Describe the morphology of the erythrocytes.
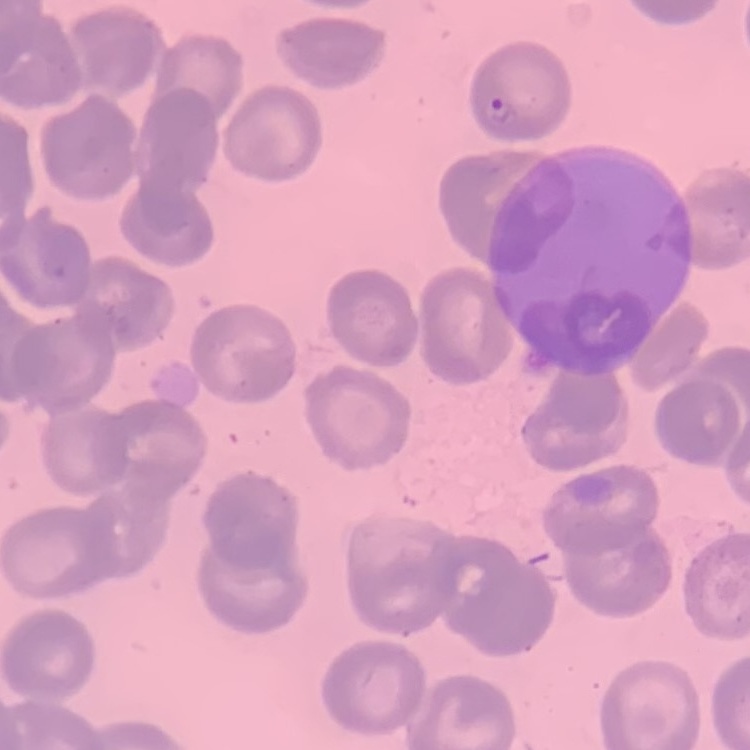

They show no rouleaux formation.

Stained with either Field's or Giemsa. One tile cut from a larger photomicrograph. Thin peripheral smear.